Identify the parasite.
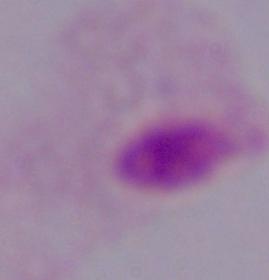
A trichomonad.

magnification = 1000x
modality = photomicrograph